Assess the morphology of the red blood cells.
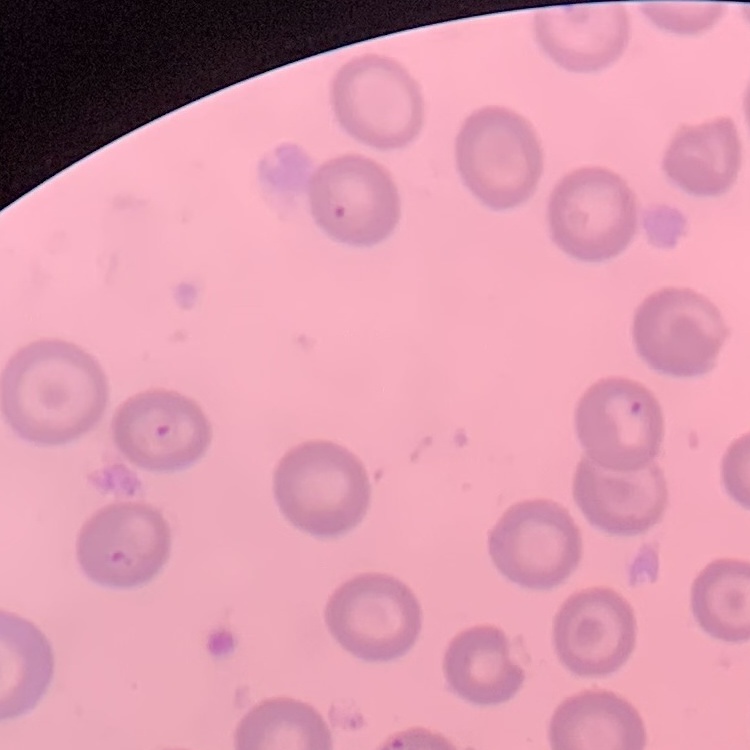

No rouleaux formation.

Summary:
  - Image type: one tile cut from a larger photomicrograph
  - Preparation: thin blood smear
  - Stain: Field's or Giemsa